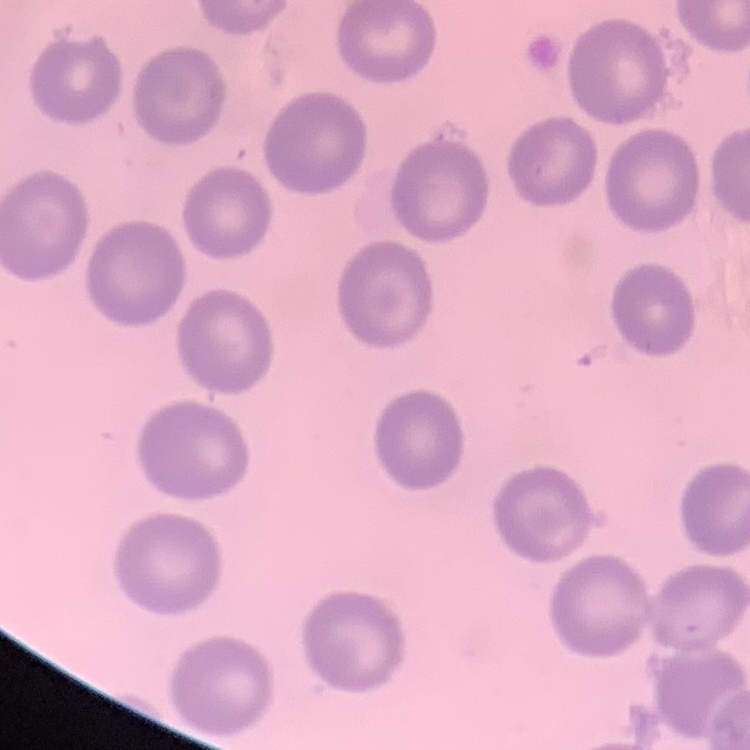

Summary:
  - Erythrocyte morphology: no rouleaux formation
  - Preparation: thin peripheral smear
  - Image type: one tile cut from a larger photomicrograph
  - Stain: Field's or Giemsa